Classify this cell by malaria status.
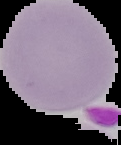

It is uninfected.

Summary:
  - Image size: 121×145 pixels
  - Preparation: thin blood film
  - Image type: segmented cell region with the area outside set to black